Point out each Plasmodium parasite and each leukocyte.
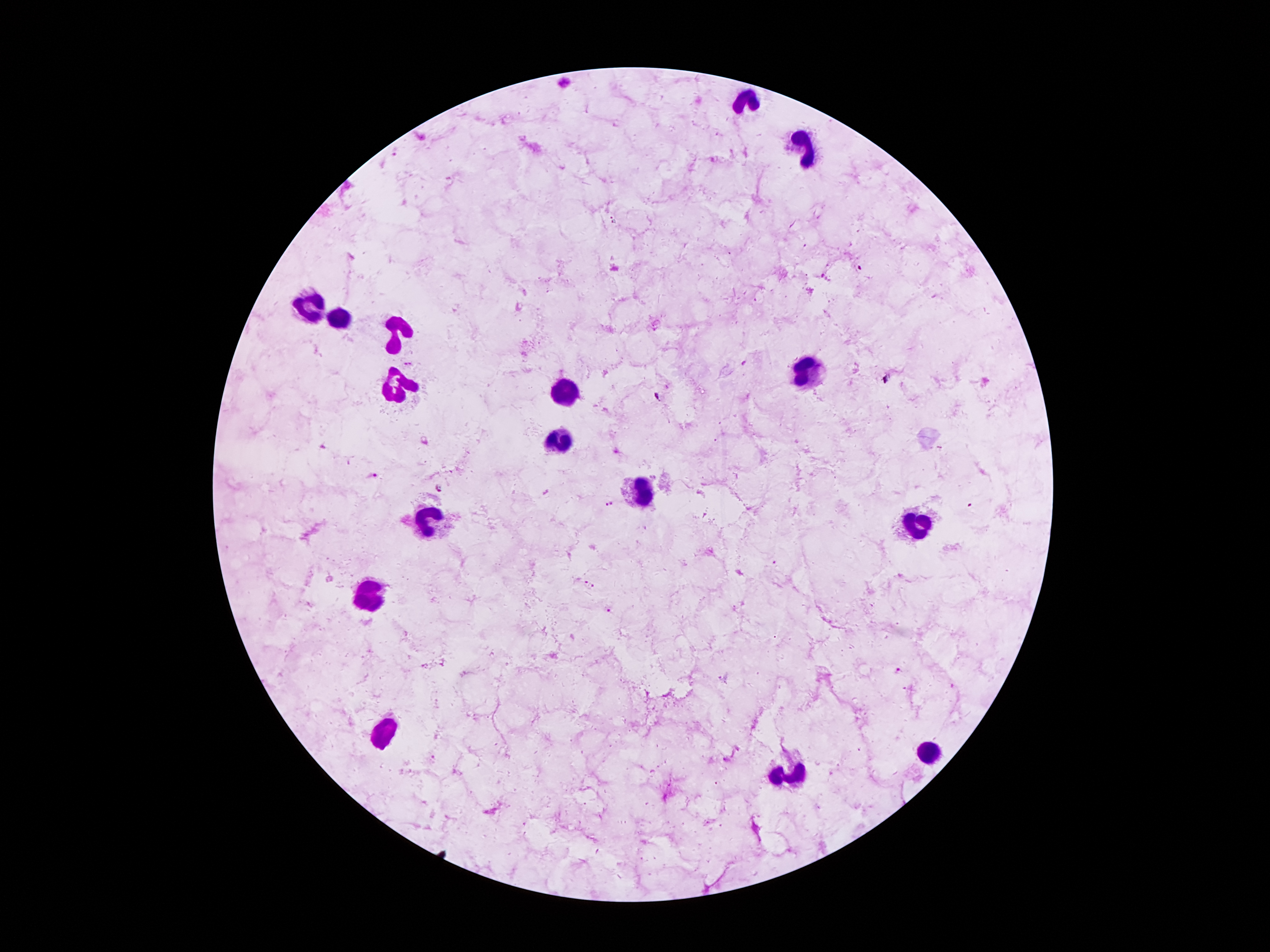

Approximate centers as (x, y) in pixels.
Plasmodium parasites: (396, 149), (408, 364), (658, 396), (323, 447), (372, 475), (439, 488), (609, 502), (589, 584), (897, 671).
Leukocytes: (747, 97), (806, 145), (308, 306), (342, 317), (398, 332), (812, 374), (398, 388), (566, 388), (558, 437), (646, 485), (428, 518), (913, 525), (367, 596), (386, 728), (925, 754), (789, 772).

patient malaria status = infected with Plasmodium falciparum
stain = Giemsa
image size = 1270×952 pixels
preparation = thick blood smear
field of view = single
capture = smartphone through the microscope eyepiece
magnification = 100x